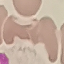
{
  "result": "no malaria parasites detected",
  "stain": "Giemsa",
  "preparation": "thin smear",
  "image_type": "cell patch, automatically extracted from a larger field of view and resized to 64 × 64 pixels",
  "capture": "smartphone through the microscope eyepiece"
}